Classify this cell by malaria status.
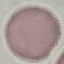

Uninfected.

Summary:
  - Image type: automatically extracted cell patch, resized to 64 × 64 pixels
  - Stain: Giemsa
  - Capture: smartphone camera at the microscope eyepiece
  - Preparation: thin blood smear